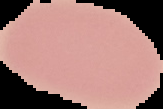

Malaria status: uninfected. From a thin blood smear. Image is 163×109 pixels. The area outside the segmented cell region is set to black.